Name the blood parasite species.
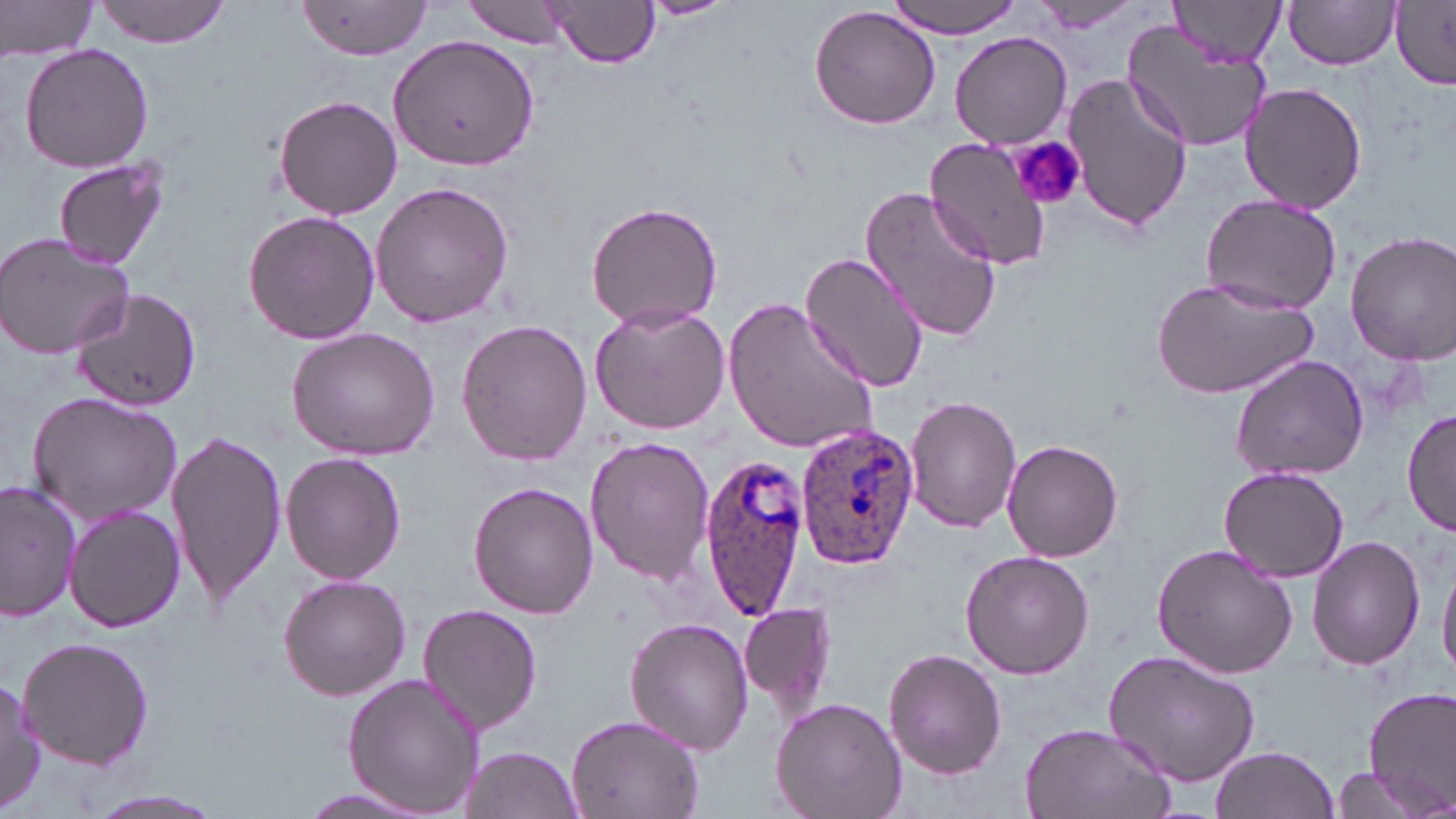

Plasmodium ovale.

stain: May-Grünwald-Giemsa
plasmodium_ovale_infected_red_blood_cell_locations: 'approximate bounding boxes as named x1/y1/x2/y2 corners in pixels: (x1=795, y1=424, x2=918, y2=569), (x1=698, y1=452, x2=812, y2=618)'
magnification: 1000x
field_of_view: single
preparation: thin blood film
modality: light microscopy
uninfected_red_blood_cell_locations: 'approximate bounding boxes as named x1/y1/x2/y2 corners in pixels: (x1=0, y1=0, x2=101, y2=60), (x1=94, y1=0, x2=230, y2=46), (x1=639, y1=0, x2=735, y2=19), (x1=892, y1=0, x2=1023, y2=37), (x1=1028, y1=0, x2=1142, y2=31), (x1=1172, y1=0, x2=1285, y2=68), (x1=462, y1=1, x2=572, y2=48), (x1=1282, y1=1, x2=1401, y2=71), (x1=1389, y1=1, x2=1456, y2=89), (x1=296, y1=2, x2=433, y2=59), (x1=545, y1=2, x2=659, y2=69), (x1=809, y1=7, x2=940, y2=130), (x1=1122, y1=20, x2=1271, y2=154), (x1=389, y1=31, x2=540, y2=172), (x1=950, y1=33, x2=1072, y2=148), (x1=18, y1=42, x2=155, y2=174), (x1=1063, y1=74, x2=1192, y2=234), (x1=1238, y1=80, x2=1367, y2=214), (x1=272, y1=94, x2=403, y2=220), (x1=924, y1=136, x2=1054, y2=270), (x1=53, y1=157, x2=169, y2=271), (x1=369, y1=180, x2=516, y2=329), (x1=860, y1=185, x2=1002, y2=344), (x1=1198, y1=192, x2=1344, y2=314), (x1=586, y1=200, x2=724, y2=331), (x1=243, y1=208, x2=380, y2=346), (x1=1346, y1=231, x2=1456, y2=363), (x1=0, y1=232, x2=135, y2=360), (x1=800, y1=248, x2=930, y2=394), (x1=1150, y1=276, x2=1318, y2=402), (x1=69, y1=289, x2=202, y2=409), (x1=725, y1=295, x2=881, y2=458), (x1=590, y1=300, x2=733, y2=435), (x1=454, y1=318, x2=592, y2=464), (x1=284, y1=326, x2=442, y2=461), (x1=1230, y1=353, x2=1371, y2=483), (x1=26, y1=390, x2=183, y2=526), (x1=905, y1=395, x2=1022, y2=533), (x1=1403, y1=408, x2=1456, y2=541), (x1=166, y1=426, x2=287, y2=610), (x1=584, y1=434, x2=714, y2=588), (x1=1001, y1=439, x2=1124, y2=563), (x1=281, y1=452, x2=406, y2=585), (x1=1219, y1=465, x2=1351, y2=582), (x1=0, y1=481, x2=79, y2=621), (x1=469, y1=481, x2=599, y2=618), (x1=1172, y1=489, x2=1322, y2=647), (x1=65, y1=504, x2=186, y2=633), (x1=1309, y1=534, x2=1426, y2=670), (x1=1152, y1=542, x2=1299, y2=679), (x1=960, y1=550, x2=1095, y2=680), (x1=1438, y1=555, x2=1456, y2=682), (x1=277, y1=573, x2=411, y2=701), (x1=740, y1=599, x2=837, y2=717), (x1=416, y1=603, x2=544, y2=734), (x1=626, y1=616, x2=753, y2=756), (x1=16, y1=635, x2=155, y2=769), (x1=884, y1=647, x2=1006, y2=777), (x1=1103, y1=650, x2=1261, y2=787), (x1=342, y1=674, x2=486, y2=815), (x1=0, y1=677, x2=45, y2=814), (x1=1363, y1=688, x2=1456, y2=811), (x1=770, y1=696, x2=907, y2=819), (x1=566, y1=712, x2=706, y2=819), (x1=1020, y1=721, x2=1175, y2=819), (x1=461, y1=746, x2=584, y2=818), (x1=1210, y1=746, x2=1340, y2=819), (x1=1325, y1=765, x2=1439, y2=819), (x1=76, y1=786, x2=233, y2=819), (x1=294, y1=786, x2=434, y2=816)'
platelet_locations: 'approximate bounding boxes as named x1/y1/x2/y2 corners in pixels: (x1=1008, y1=135, x2=1087, y2=213)'
image_size: 1456×819 pixels